Classify this cell by malaria status.
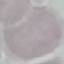

Uninfected.

Acquired by smartphone through the microscope eyepiece. Giemsa stain. Thin blood smear. Automatically extracted cell patch, resized to 64 × 64 pixels.